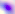
Summary:
  - Identification: Toxoplasma gondii
  - Magnification: 400x
  - Modality: photomicrograph